Classify this cell by malaria status.
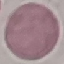

It is uninfected.

{
  "stain": "Giemsa",
  "image_type": "cell patch, automatically extracted from a larger field of view and resized to 64 × 64 pixels",
  "capture": "smartphone through the microscope eyepiece",
  "preparation": "thin blood smear"
}